Identify the parasite.
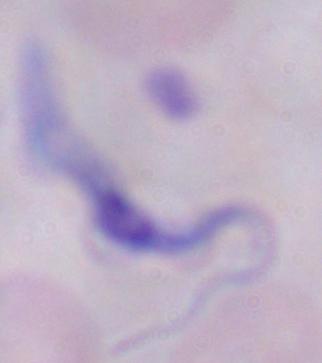
This is a trypanosome.

modality = photomicrograph
magnification = 1000x